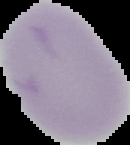

preparation = thin blood smear
malaria status = uninfected
image type = segmented cell region on a black background
image size = 130×145 pixels